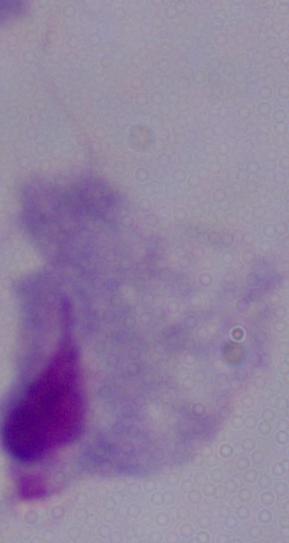
A trichomonad is seen. Captured at 1000x magnification. Photomicrograph.